Name the parasite shown.
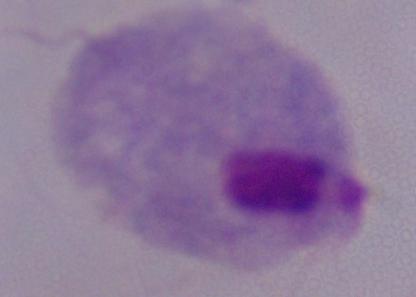

This is a trichomonad.

Summary:
  - Magnification: 1000x
  - Modality: micrograph